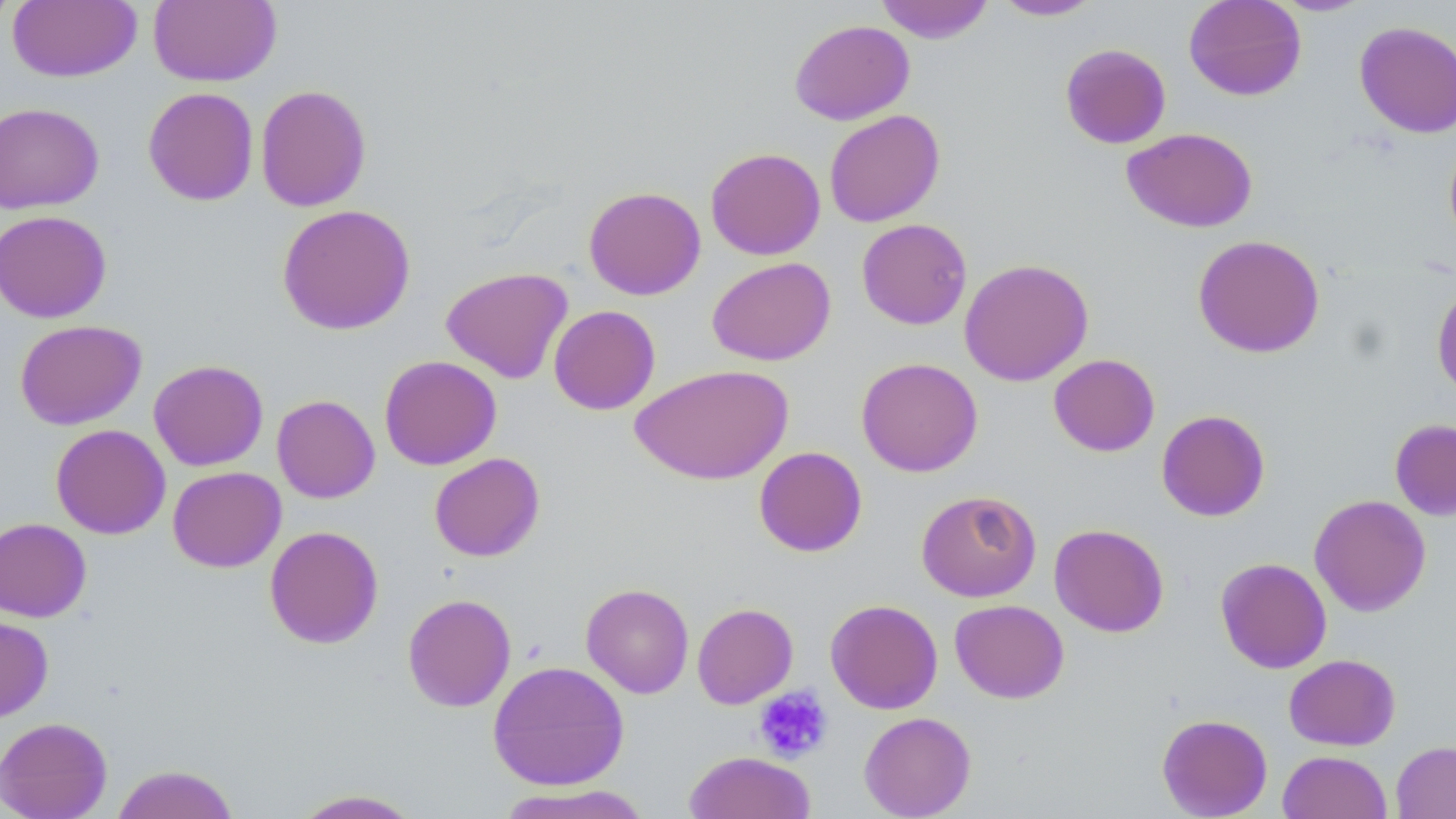
Approximate bounding boxes as named x1/y1/x2/y2 corners in pixels. Uninfected red blood cell locations: (x1=0, y1=0, x2=18, y2=30), (x1=148, y1=0, x2=281, y2=87), (x1=875, y1=0, x2=994, y2=43), (x1=993, y1=0, x2=1102, y2=21), (x1=1183, y1=0, x2=1307, y2=101), (x1=1271, y1=0, x2=1375, y2=16), (x1=8, y1=1, x2=141, y2=83), (x1=790, y1=19, x2=914, y2=125), (x1=1354, y1=21, x2=1456, y2=138), (x1=1060, y1=43, x2=1171, y2=149), (x1=255, y1=84, x2=371, y2=212), (x1=143, y1=87, x2=259, y2=206), (x1=0, y1=102, x2=104, y2=214), (x1=824, y1=109, x2=945, y2=227), (x1=1121, y1=127, x2=1258, y2=233), (x1=1443, y1=135, x2=1456, y2=250), (x1=705, y1=147, x2=825, y2=260), (x1=583, y1=186, x2=706, y2=300), (x1=276, y1=204, x2=416, y2=335), (x1=0, y1=210, x2=112, y2=323), (x1=856, y1=218, x2=972, y2=330), (x1=1192, y1=234, x2=1325, y2=358), (x1=707, y1=257, x2=835, y2=366), (x1=959, y1=258, x2=1094, y2=386), (x1=440, y1=266, x2=573, y2=384), (x1=1431, y1=282, x2=1456, y2=399), (x1=548, y1=305, x2=661, y2=415), (x1=15, y1=319, x2=146, y2=430), (x1=1048, y1=354, x2=1160, y2=456), (x1=379, y1=355, x2=502, y2=470), (x1=856, y1=357, x2=983, y2=477), (x1=148, y1=359, x2=268, y2=471), (x1=631, y1=364, x2=793, y2=485), (x1=272, y1=395, x2=380, y2=503), (x1=1156, y1=409, x2=1270, y2=522), (x1=1389, y1=418, x2=1456, y2=521), (x1=51, y1=424, x2=170, y2=539), (x1=753, y1=446, x2=867, y2=556), (x1=429, y1=453, x2=545, y2=562), (x1=167, y1=466, x2=286, y2=572), (x1=916, y1=489, x2=1041, y2=602), (x1=1309, y1=494, x2=1432, y2=616), (x1=0, y1=518, x2=91, y2=622), (x1=1049, y1=523, x2=1169, y2=637), (x1=264, y1=525, x2=383, y2=649), (x1=1215, y1=557, x2=1332, y2=673), (x1=581, y1=583, x2=694, y2=698), (x1=402, y1=593, x2=517, y2=712), (x1=825, y1=599, x2=943, y2=714), (x1=950, y1=599, x2=1069, y2=703), (x1=692, y1=602, x2=798, y2=709), (x1=0, y1=615, x2=53, y2=723), (x1=1283, y1=654, x2=1400, y2=751), (x1=488, y1=660, x2=630, y2=791), (x1=859, y1=711, x2=976, y2=818), (x1=1157, y1=713, x2=1273, y2=818), (x1=0, y1=716, x2=112, y2=819), (x1=1391, y1=741, x2=1456, y2=818), (x1=1277, y1=750, x2=1392, y2=819), (x1=683, y1=751, x2=816, y2=819), (x1=111, y1=764, x2=240, y2=819), (x1=494, y1=784, x2=654, y2=819), (x1=290, y1=788, x2=424, y2=818). Platelet locations: (x1=754, y1=686, x2=832, y2=762). Slide-level diagnosis: no evidence of blood parasites. One field of a larger specimen. Captured at 1000x magnification. Image is 1456×819 pixels. Thin blood smear. Light microscopy. May-Grünwald-Giemsa-stained preparation.